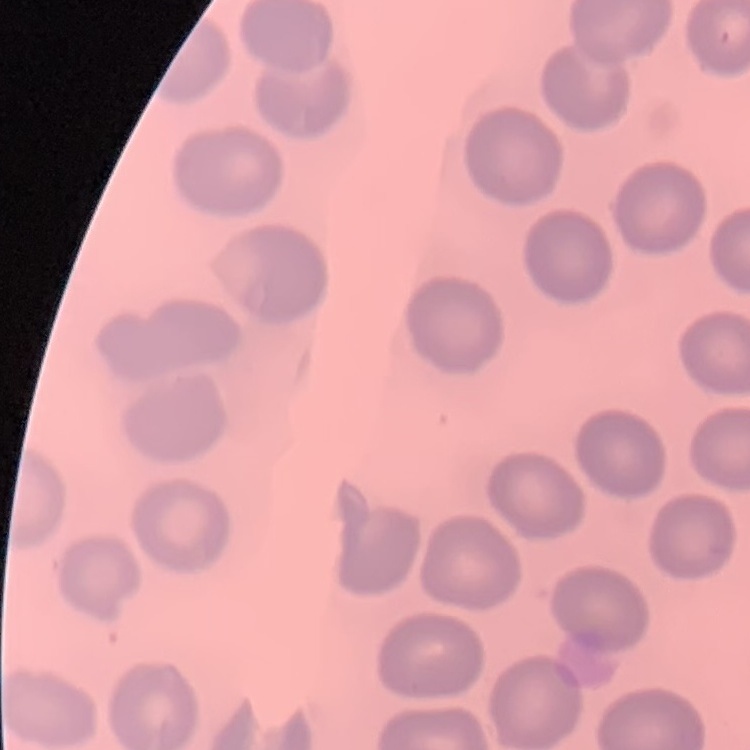
red_blood_cell_morphology: no rouleaux formation
image_type: square crop of a larger photomicrograph
stain: Field's or Giemsa
preparation: thin blood smear